Report the malaria status of this cell.
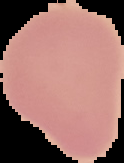
Uninfected.

Summary:
  - Image size: 124×163 pixels
  - Preparation: thin blood film
  - Image type: segmented cell region with the area outside set to black